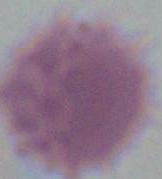

magnification = 1000x
modality = micrograph
identification = red blood cell